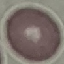

Summary:
  - Result: negative for malaria parasites
  - Capture: smartphone through the microscope eyepiece
  - Preparation: thin blood smear
  - Stain: Giemsa
  - Image type: automatically extracted cell patch, resized to 64 × 64 pixels